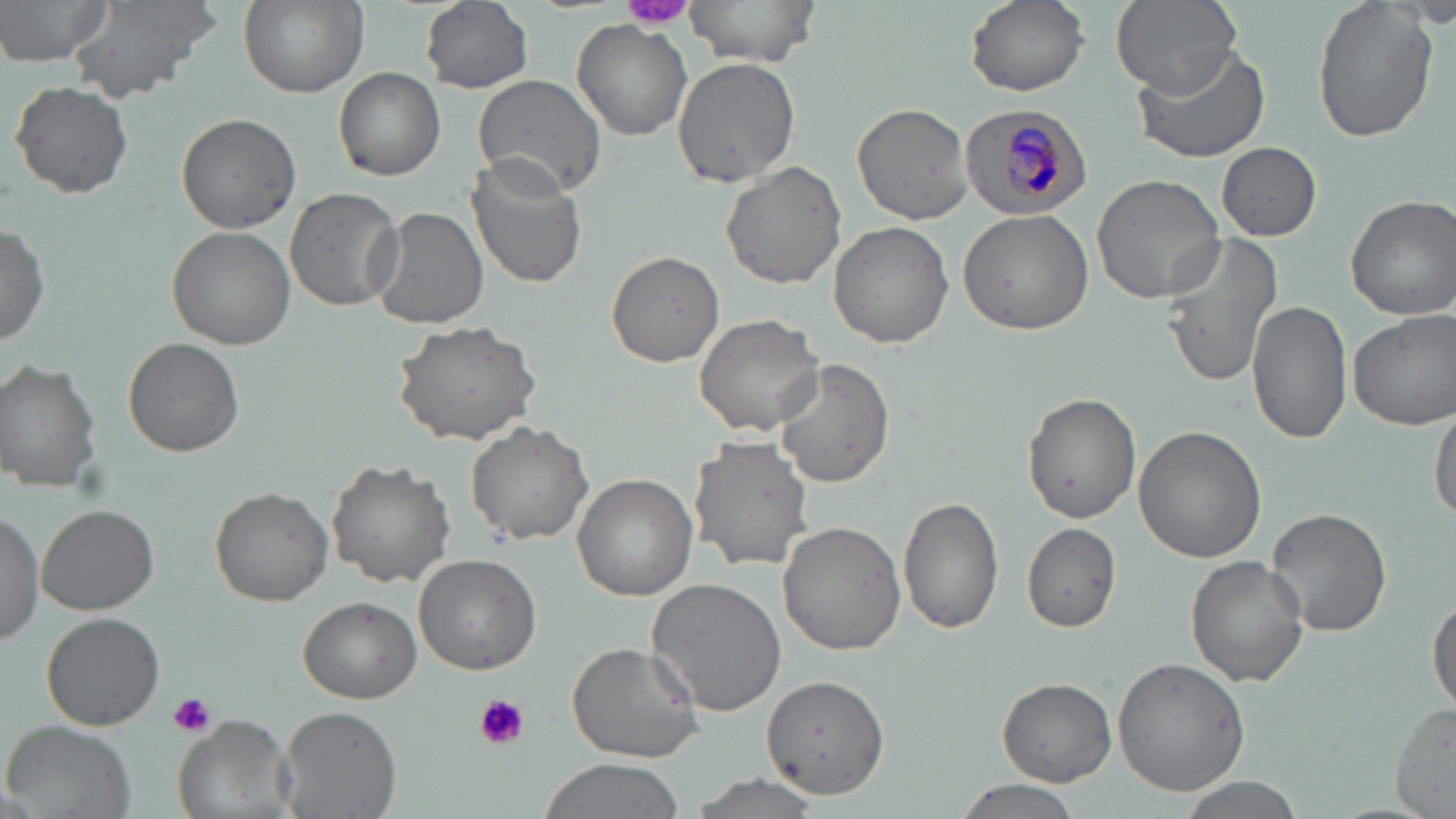

Approximate bounding boxes as named x1/y1/x2/y2 corners in pixels. Plasmodium malariae-infected red blood cell locations: (x1=959, y1=103, x2=1093, y2=219). Uninfected red blood cell locations: (x1=0, y1=0, x2=115, y2=68), (x1=68, y1=0, x2=221, y2=106), (x1=237, y1=0, x2=367, y2=98), (x1=418, y1=0, x2=536, y2=95), (x1=682, y1=0, x2=823, y2=67), (x1=964, y1=0, x2=1089, y2=96), (x1=1109, y1=0, x2=1245, y2=101), (x1=1312, y1=0, x2=1438, y2=142), (x1=1403, y1=5, x2=1456, y2=31), (x1=571, y1=19, x2=692, y2=140), (x1=1129, y1=43, x2=1272, y2=165), (x1=672, y1=57, x2=801, y2=187), (x1=334, y1=66, x2=446, y2=181), (x1=472, y1=73, x2=607, y2=196), (x1=11, y1=81, x2=133, y2=199), (x1=851, y1=102, x2=976, y2=225), (x1=176, y1=113, x2=301, y2=234), (x1=1216, y1=143, x2=1321, y2=240), (x1=463, y1=155, x2=588, y2=291), (x1=720, y1=162, x2=847, y2=290), (x1=1092, y1=172, x2=1225, y2=304), (x1=285, y1=187, x2=404, y2=312), (x1=1346, y1=195, x2=1456, y2=320), (x1=368, y1=206, x2=489, y2=331), (x1=957, y1=209, x2=1095, y2=335), (x1=0, y1=221, x2=50, y2=345), (x1=828, y1=221, x2=954, y2=350), (x1=166, y1=226, x2=298, y2=348), (x1=1158, y1=232, x2=1287, y2=386), (x1=607, y1=251, x2=726, y2=368), (x1=1247, y1=300, x2=1354, y2=444), (x1=1349, y1=310, x2=1455, y2=430), (x1=693, y1=311, x2=825, y2=437), (x1=393, y1=319, x2=543, y2=445), (x1=123, y1=337, x2=245, y2=457), (x1=773, y1=357, x2=894, y2=488), (x1=0, y1=360, x2=104, y2=492), (x1=1022, y1=393, x2=1141, y2=523), (x1=1429, y1=398, x2=1456, y2=527), (x1=466, y1=420, x2=593, y2=544), (x1=1133, y1=425, x2=1266, y2=562), (x1=690, y1=437, x2=814, y2=573), (x1=327, y1=460, x2=456, y2=589), (x1=571, y1=474, x2=697, y2=601), (x1=209, y1=485, x2=334, y2=607), (x1=898, y1=496, x2=1006, y2=636), (x1=38, y1=504, x2=159, y2=615), (x1=1267, y1=506, x2=1392, y2=638), (x1=0, y1=509, x2=45, y2=644), (x1=778, y1=520, x2=907, y2=655), (x1=1021, y1=523, x2=1122, y2=633), (x1=413, y1=553, x2=543, y2=676), (x1=1186, y1=555, x2=1310, y2=687), (x1=647, y1=577, x2=789, y2=716), (x1=1429, y1=593, x2=1456, y2=712), (x1=298, y1=598, x2=421, y2=704), (x1=40, y1=612, x2=166, y2=731), (x1=565, y1=640, x2=703, y2=763), (x1=1113, y1=656, x2=1251, y2=795), (x1=762, y1=673, x2=890, y2=799), (x1=997, y1=677, x2=1116, y2=785), (x1=1389, y1=703, x2=1456, y2=817), (x1=278, y1=705, x2=403, y2=818), (x1=173, y1=713, x2=298, y2=819), (x1=4, y1=720, x2=136, y2=818), (x1=537, y1=757, x2=686, y2=818), (x1=684, y1=776, x2=821, y2=819), (x1=950, y1=777, x2=1086, y2=819), (x1=1176, y1=777, x2=1304, y2=818). Platelet locations: (x1=619, y1=0, x2=696, y2=30), (x1=167, y1=692, x2=217, y2=737), (x1=472, y1=692, x2=530, y2=751). Slide-level diagnosis: Plasmodium malariae. May-Grünwald-Giemsa stain. Image is 1456×819 pixels. Optical microscopy. 1000x magnification. Thin blood film. One field of a larger specimen.